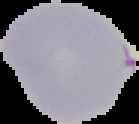

image_size: 139×124 pixels
image_type: cell region segmented out of the field of view; surrounding area masked to black
preparation: thin blood film
result: malaria parasites detected